Name the parasite shown.
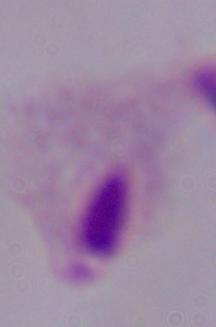
This is a trichomonad.

Photomicrograph. Captured at 1000x magnification.